Classify this cell by malaria status.
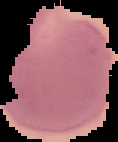

It is parasitized.

Summary:
  - Preparation: thin blood film
  - Image size: 118×142 pixels
  - Image type: segmented cell region on a black background